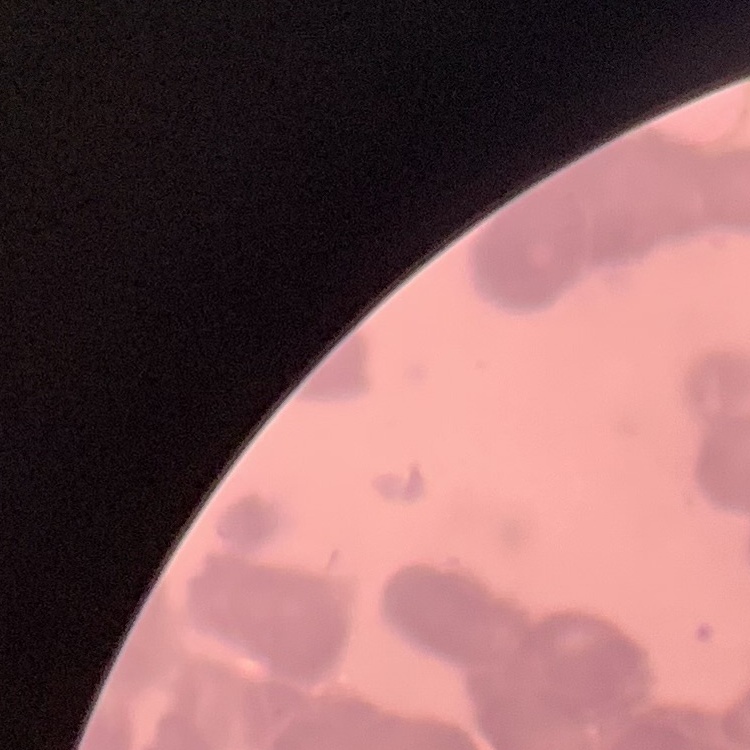

{
  "erythrocyte_morphology": "rouleaux formation",
  "image_type": "square crop of a larger photomicrograph",
  "preparation": "thin peripheral smear",
  "stain": "Field's or Giemsa"
}